State the blood parasite species.
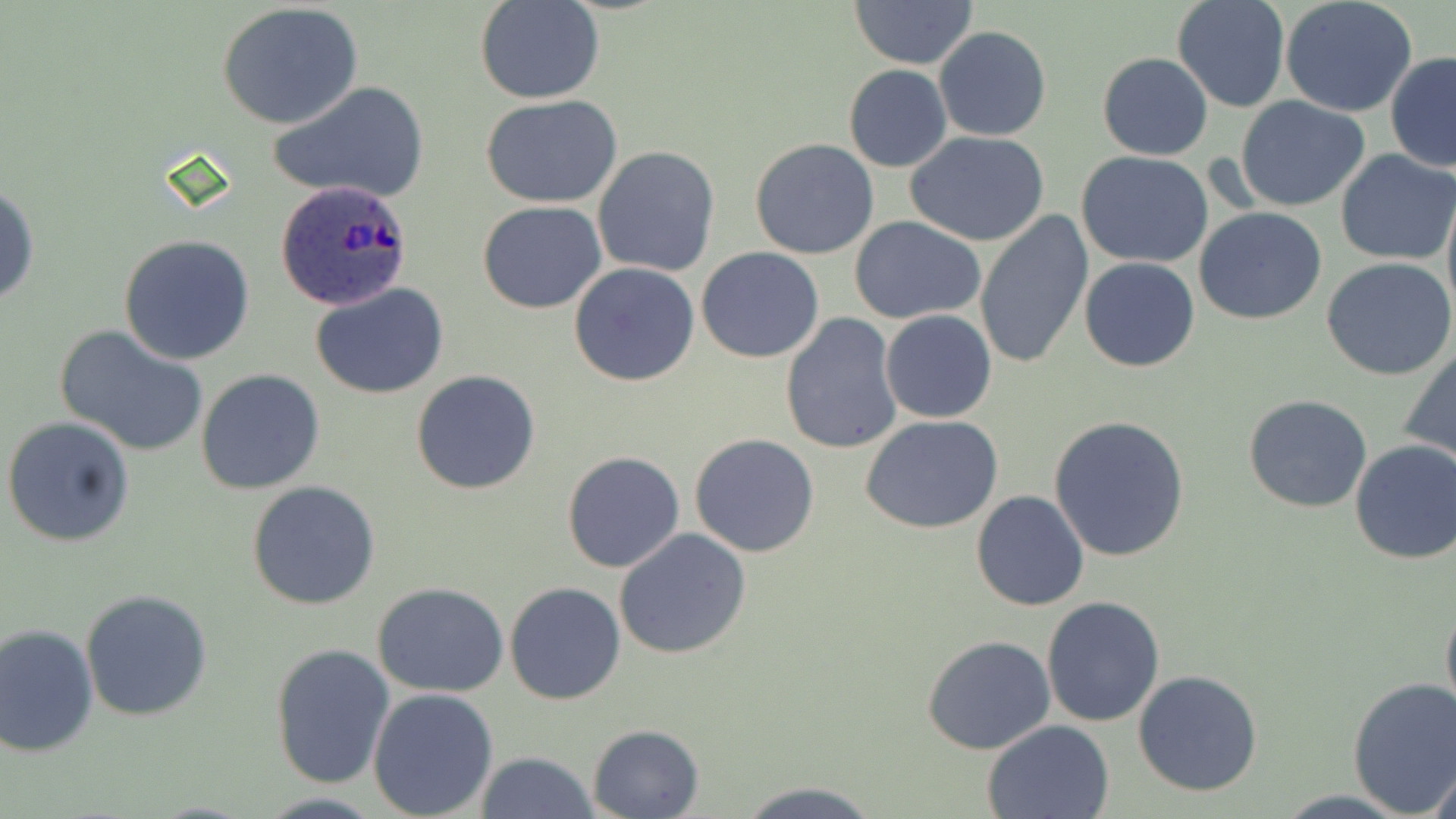

Plasmodium ovale.

Approximate bounding boxes as named x1/y1/x2/y2 corners in pixels. Plasmodium ovale-infected red blood cell locations: (x1=274, y1=182, x2=413, y2=311). Uninfected red blood cell locations: (x1=474, y1=0, x2=605, y2=104), (x1=849, y1=0, x2=978, y2=69), (x1=1171, y1=0, x2=1290, y2=112), (x1=1280, y1=0, x2=1417, y2=117), (x1=216, y1=3, x2=365, y2=129), (x1=933, y1=26, x2=1053, y2=143), (x1=1097, y1=51, x2=1213, y2=161), (x1=1385, y1=52, x2=1456, y2=173), (x1=842, y1=64, x2=951, y2=173), (x1=270, y1=82, x2=429, y2=206), (x1=480, y1=94, x2=627, y2=206), (x1=1234, y1=96, x2=1371, y2=211), (x1=904, y1=129, x2=1051, y2=245), (x1=750, y1=137, x2=878, y2=259), (x1=592, y1=145, x2=721, y2=278), (x1=1335, y1=150, x2=1455, y2=263), (x1=1076, y1=151, x2=1214, y2=269), (x1=1, y1=179, x2=39, y2=311), (x1=1441, y1=185, x2=1456, y2=328), (x1=477, y1=202, x2=606, y2=315), (x1=1194, y1=207, x2=1327, y2=325), (x1=973, y1=211, x2=1093, y2=371), (x1=850, y1=217, x2=988, y2=323), (x1=118, y1=234, x2=256, y2=365), (x1=696, y1=247, x2=825, y2=363), (x1=1079, y1=258, x2=1200, y2=371), (x1=1322, y1=258, x2=1456, y2=382), (x1=569, y1=263, x2=699, y2=386), (x1=312, y1=284, x2=450, y2=400), (x1=880, y1=309, x2=997, y2=423), (x1=780, y1=312, x2=903, y2=454), (x1=57, y1=326, x2=210, y2=458), (x1=1401, y1=343, x2=1456, y2=467), (x1=196, y1=370, x2=326, y2=495), (x1=411, y1=370, x2=542, y2=495), (x1=1242, y1=394, x2=1373, y2=513), (x1=3, y1=415, x2=135, y2=548), (x1=1049, y1=415, x2=1190, y2=562), (x1=862, y1=417, x2=1005, y2=534), (x1=689, y1=433, x2=820, y2=557), (x1=1348, y1=439, x2=1456, y2=565), (x1=561, y1=451, x2=686, y2=574), (x1=248, y1=480, x2=381, y2=611), (x1=970, y1=490, x2=1090, y2=611), (x1=612, y1=529, x2=753, y2=661), (x1=505, y1=581, x2=626, y2=706), (x1=372, y1=583, x2=511, y2=698), (x1=80, y1=590, x2=214, y2=722), (x1=1440, y1=594, x2=1456, y2=729), (x1=1041, y1=596, x2=1166, y2=726), (x1=0, y1=623, x2=100, y2=757), (x1=923, y1=635, x2=1056, y2=755), (x1=269, y1=641, x2=396, y2=790), (x1=1132, y1=670, x2=1263, y2=797), (x1=1346, y1=676, x2=1456, y2=816), (x1=367, y1=687, x2=498, y2=819), (x1=982, y1=719, x2=1115, y2=818), (x1=586, y1=724, x2=704, y2=818), (x1=474, y1=751, x2=596, y2=819), (x1=1426, y1=755, x2=1455, y2=818), (x1=738, y1=781, x2=879, y2=818). One field of a larger specimen. Captured at 1000x magnification. Image is 1456×819 pixels. May-Grünwald-Giemsa-stained preparation. Thin blood film. Light microscopy.